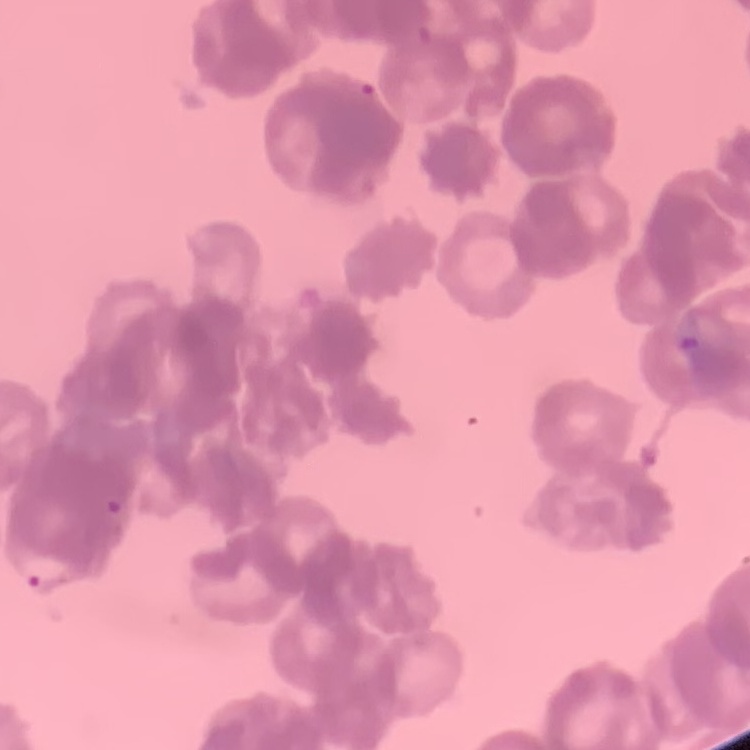

Summary:
  - Red blood cell morphology: rouleaux formation
  - Stain: Field's or Giemsa
  - Preparation: thin peripheral smear
  - Image type: one tile cut from a larger photomicrograph